Assess this cell for malaria.
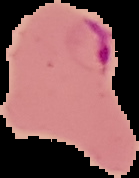

Parasitized.

Summary:
  - Image type: segmented cell region on a black background
  - Preparation: thin blood smear
  - Image size: 139×178 pixels